Look for Plasmodium parasites.
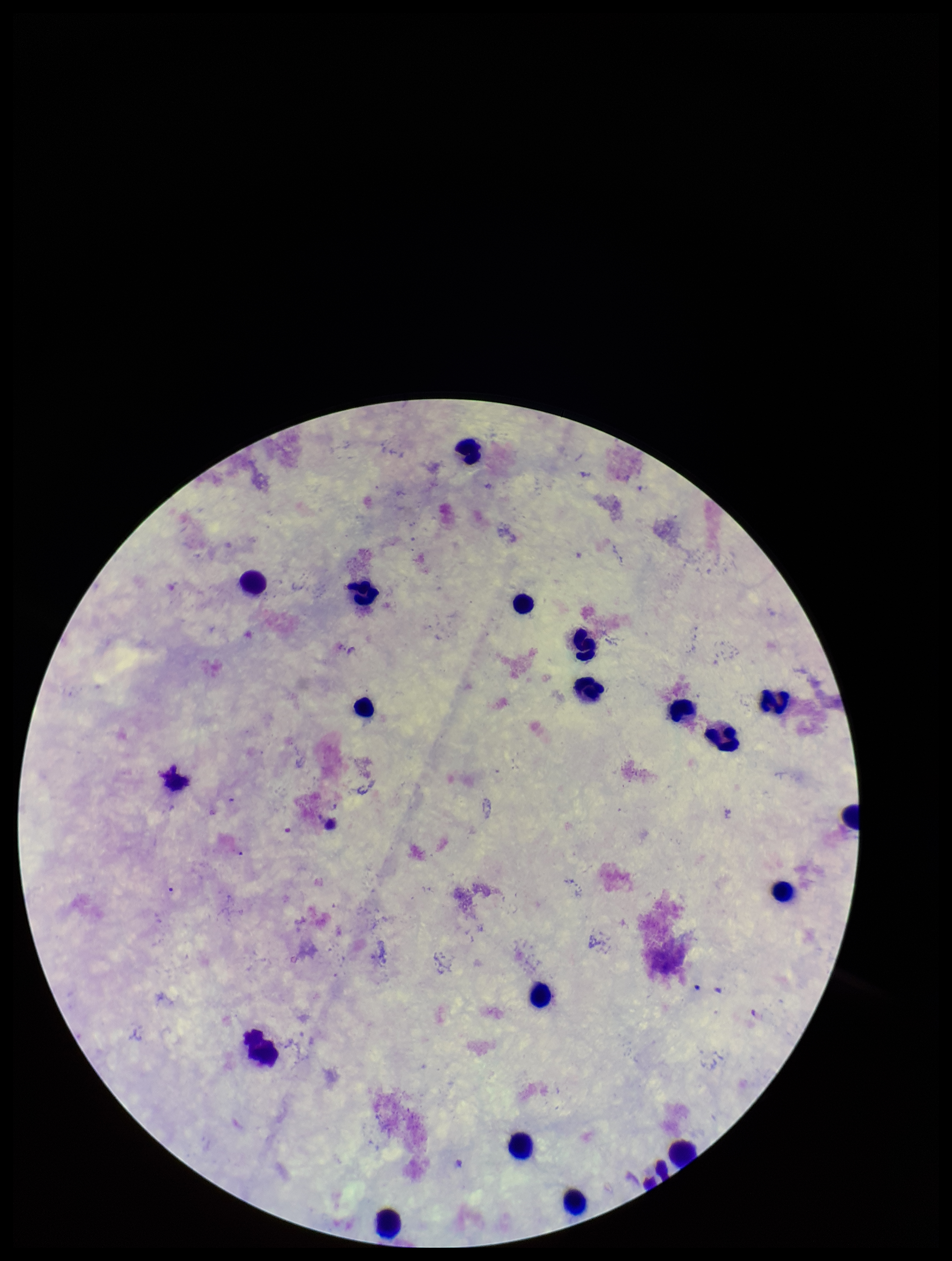

None detected.

One field from this slide. Patient malaria status: negative. Leukocyte count: 17. Image is 952×1261 pixels. Preparation: thick. Stained with Giemsa. Parasite count: 0. Smartphone photograph taken through the eyepiece of a microscope.